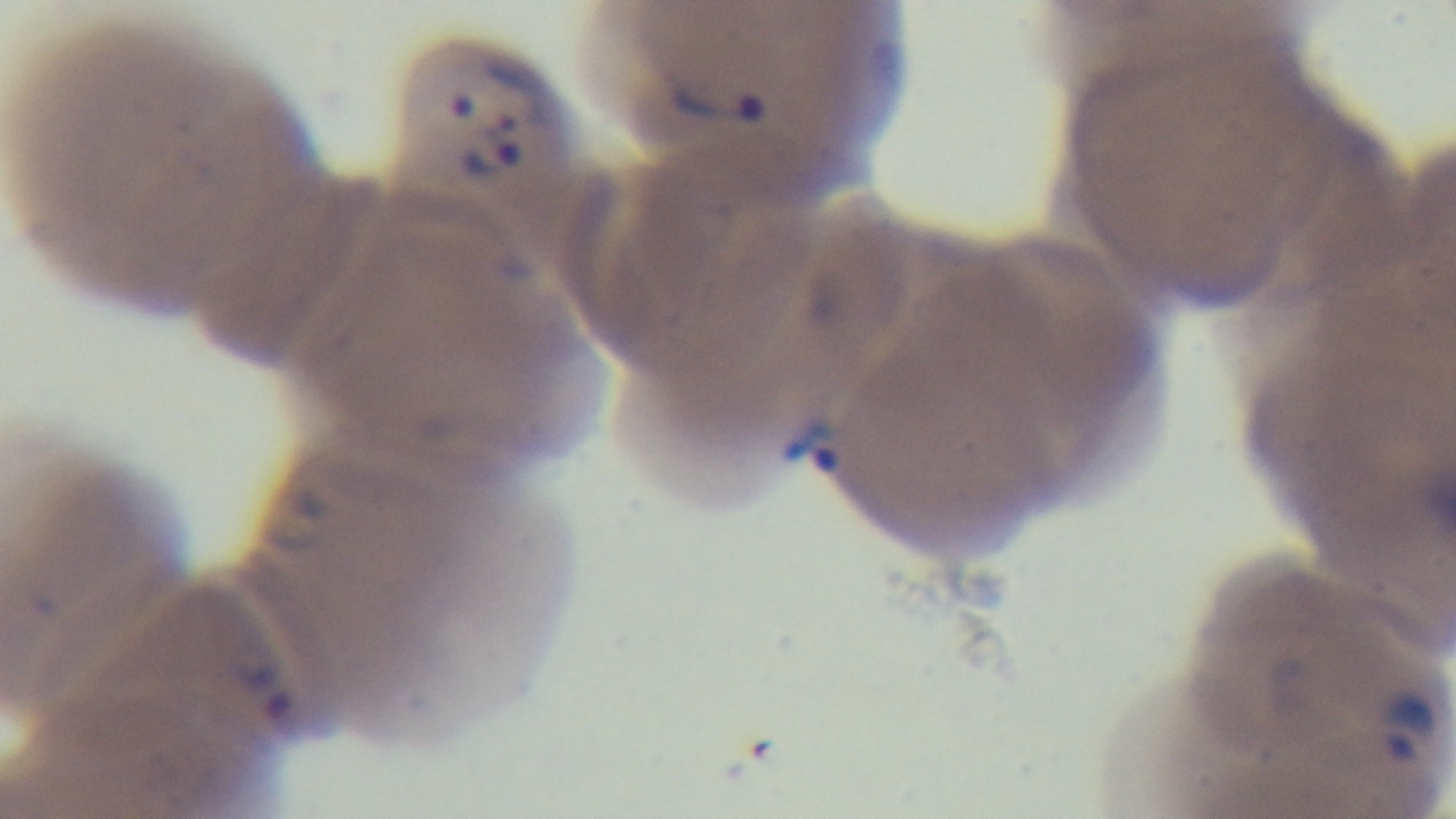

Summary:
  - Field of view: single
  - Preparation: thin blood film
  - Malaria status: positive
  - Objective: 100x oil immersion
  - Stain: Giemsa
  - Modality: light microscopy
  - Capture: mounted 4K digital camera